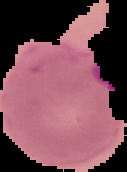

Summary:
  - Image type: segmented cell region with the area outside set to black
  - Preparation: thin blood film
  - Image size: 127×172 pixels
  - Result: Plasmodium parasites detected